State which parasite is depicted.
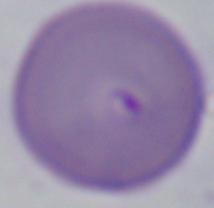

Babesia.

modality = photomicrograph
magnification = 1000x